Assess this cell for malaria.
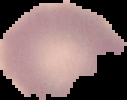
Uninfected.

From a thin blood smear. Image is 127×100 pixels. The area outside the segmented cell region is set to black.